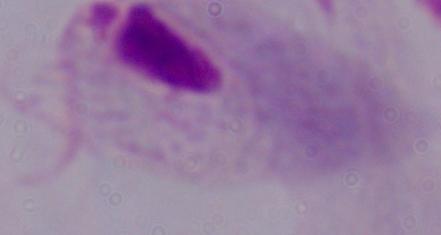
identification = trichomonad
modality = micrograph
magnification = 1000x